Assess this cell for malaria.
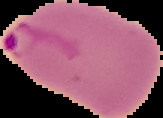

Parasitized.

Image is 163×118 pixels. From a thin blood smear. The area outside the segmented cell region is set to black.